State the blood parasite species.
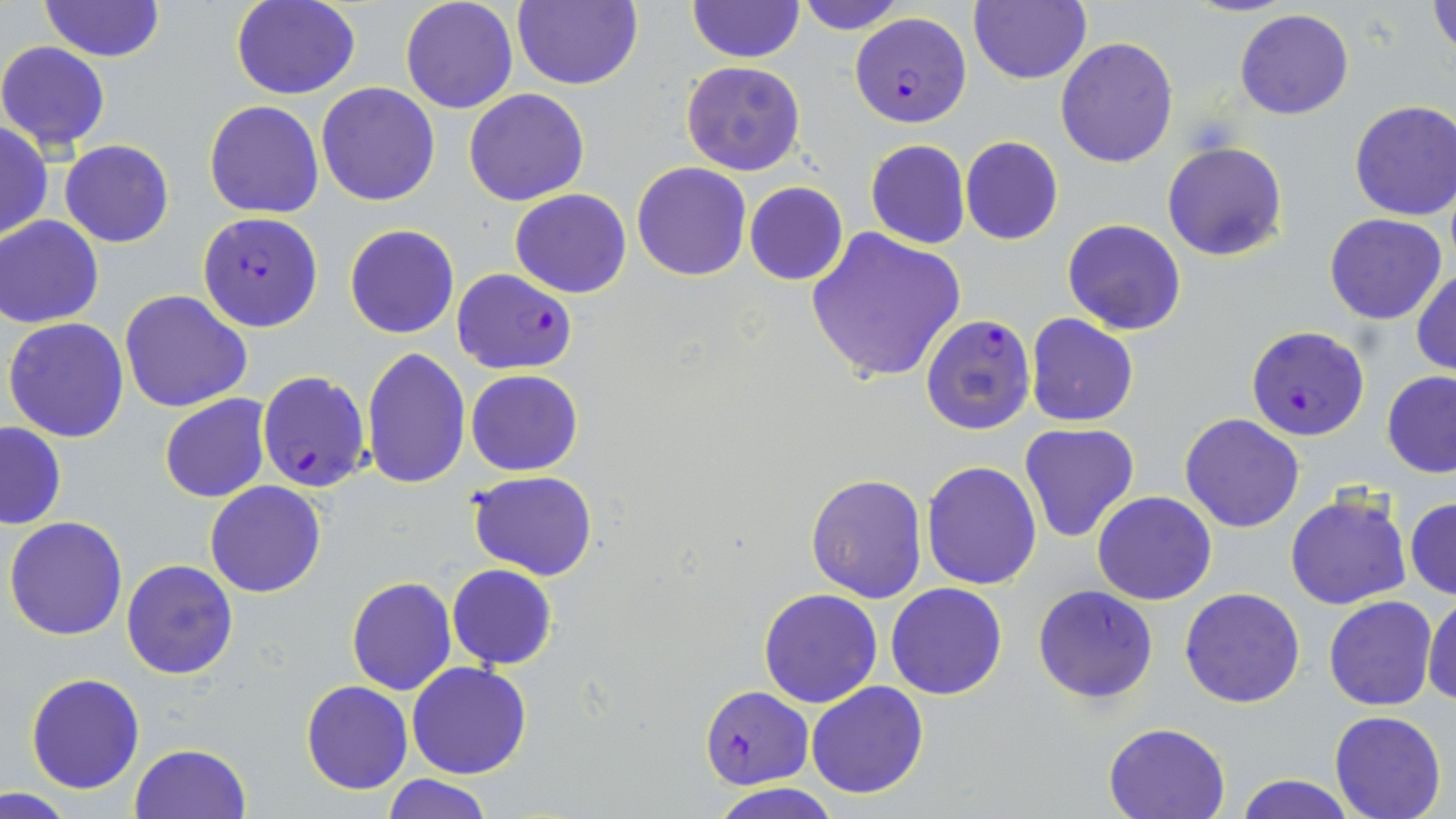

Plasmodium falciparum.

image_size: 1456×819 pixels
modality: optical microscopy
uninfected_red_blood_cell_locations: 'approximate bounding boxes as named x1/y1/x2/y2 corners in pixels: (x1=232, y1=0, x2=361, y2=100), (x1=399, y1=0, x2=520, y2=114), (x1=512, y1=0, x2=641, y2=90), (x1=688, y1=0, x2=801, y2=62), (x1=794, y1=0, x2=908, y2=33), (x1=969, y1=0, x2=1091, y2=84), (x1=1184, y1=0, x2=1299, y2=17), (x1=38, y1=1, x2=165, y2=64), (x1=1429, y1=1, x2=1455, y2=59), (x1=1234, y1=9, x2=1354, y2=121), (x1=1056, y1=38, x2=1179, y2=169), (x1=0, y1=41, x2=112, y2=152), (x1=680, y1=60, x2=806, y2=174), (x1=317, y1=82, x2=439, y2=207), (x1=464, y1=88, x2=590, y2=207), (x1=205, y1=100, x2=325, y2=219), (x1=1349, y1=100, x2=1456, y2=221), (x1=0, y1=122, x2=51, y2=244), (x1=960, y1=136, x2=1063, y2=245), (x1=865, y1=139, x2=970, y2=250), (x1=60, y1=140, x2=175, y2=248), (x1=1162, y1=141, x2=1289, y2=262), (x1=630, y1=162, x2=752, y2=281), (x1=744, y1=181, x2=849, y2=286), (x1=510, y1=188, x2=632, y2=298), (x1=1324, y1=213, x2=1448, y2=325), (x1=1, y1=216, x2=104, y2=327), (x1=1061, y1=219, x2=1186, y2=336), (x1=344, y1=224, x2=459, y2=340), (x1=804, y1=227, x2=967, y2=385), (x1=1411, y1=267, x2=1456, y2=377), (x1=120, y1=290, x2=253, y2=413), (x1=1025, y1=311, x2=1139, y2=428), (x1=4, y1=317, x2=131, y2=442), (x1=361, y1=347, x2=470, y2=489), (x1=465, y1=369, x2=583, y2=476), (x1=1381, y1=370, x2=1456, y2=476), (x1=159, y1=395, x2=271, y2=504), (x1=1179, y1=412, x2=1306, y2=532), (x1=1, y1=420, x2=66, y2=528), (x1=1018, y1=423, x2=1141, y2=542), (x1=921, y1=459, x2=1042, y2=590), (x1=466, y1=469, x2=598, y2=580), (x1=805, y1=473, x2=929, y2=603), (x1=204, y1=481, x2=327, y2=598), (x1=1091, y1=490, x2=1218, y2=605), (x1=1283, y1=493, x2=1414, y2=610), (x1=1405, y1=496, x2=1456, y2=599), (x1=5, y1=517, x2=129, y2=640), (x1=121, y1=559, x2=238, y2=680), (x1=447, y1=564, x2=557, y2=670), (x1=347, y1=577, x2=456, y2=694), (x1=885, y1=583, x2=1008, y2=700), (x1=758, y1=588, x2=883, y2=709), (x1=1179, y1=588, x2=1305, y2=709), (x1=1424, y1=594, x2=1456, y2=707), (x1=1323, y1=595, x2=1437, y2=711), (x1=406, y1=662, x2=532, y2=780), (x1=25, y1=672, x2=145, y2=793), (x1=301, y1=680, x2=414, y2=795), (x1=806, y1=681, x2=929, y2=801), (x1=1328, y1=711, x2=1447, y2=819), (x1=1103, y1=721, x2=1232, y2=819), (x1=129, y1=743, x2=253, y2=819), (x1=1235, y1=773, x2=1356, y2=818), (x1=382, y1=775, x2=492, y2=818), (x1=712, y1=783, x2=839, y2=819)'
field_of_view: single
plasmodium_falciparum_infected_red_blood_cell_locations: 'approximate bounding boxes as named x1/y1/x2/y2 corners in pixels: (x1=849, y1=11, x2=972, y2=127), (x1=197, y1=211, x2=324, y2=333), (x1=451, y1=268, x2=577, y2=376), (x1=920, y1=312, x2=1037, y2=437), (x1=1247, y1=326, x2=1370, y2=441), (x1=258, y1=369, x2=372, y2=495), (x1=1032, y1=585, x2=1159, y2=705), (x1=701, y1=686, x2=814, y2=789)'
preparation: thin blood film
stain: May-Grünwald-Giemsa
magnification: 1000x